Assess this cell for malaria.
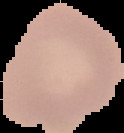
Uninfected.

preparation = thin blood smear
image size = 124×133 pixels
image type = segmented cell region with the area outside set to black